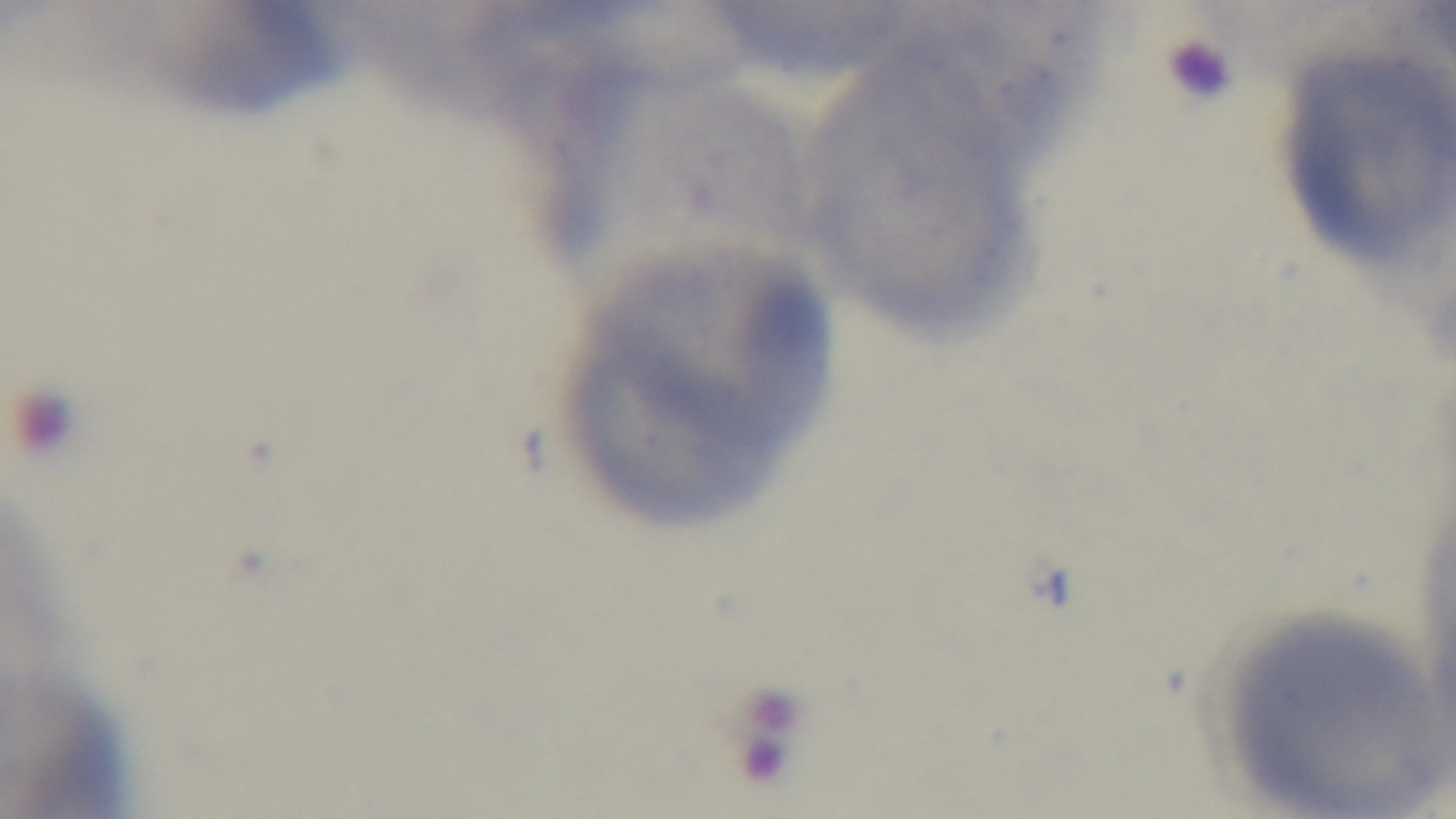
{
  "stain": "Giemsa",
  "capture": "mounted 4K digital camera",
  "objective": "100x oil immersion",
  "field_of_view": "single",
  "modality": "light microscopy",
  "preparation": "thin smear",
  "malaria_status": "uninfected"
}